State the blood parasite species.
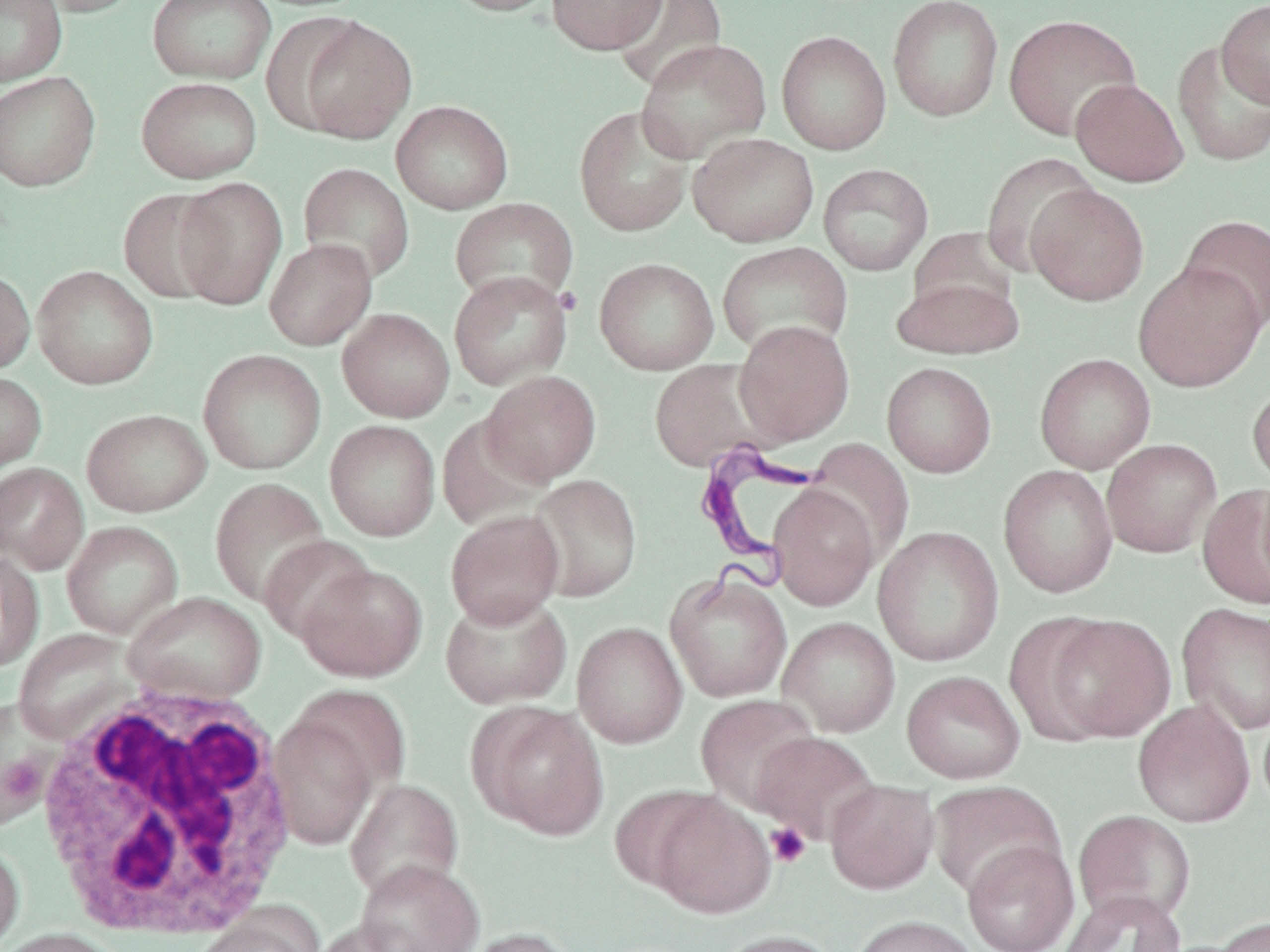

Trypanosoma brucei.

Summary:
  - Coordinate format: approximate bounding boxes as named x1/y1/x2/y2 corners in pixels
  - Trypanosoma brucei locations: (x1=687, y1=439, x2=826, y2=605)
  - Uninfected red blood cell locations: (x1=0, y1=0, x2=67, y2=86), (x1=32, y1=0, x2=144, y2=17), (x1=146, y1=0, x2=276, y2=84), (x1=442, y1=0, x2=562, y2=17), (x1=546, y1=0, x2=667, y2=54), (x1=610, y1=0, x2=728, y2=92), (x1=887, y1=0, x2=1004, y2=122), (x1=1216, y1=0, x2=1270, y2=108), (x1=1003, y1=14, x2=1141, y2=141), (x1=293, y1=15, x2=417, y2=143), (x1=776, y1=29, x2=891, y2=155), (x1=635, y1=38, x2=772, y2=163), (x1=1173, y1=41, x2=1270, y2=167), (x1=0, y1=71, x2=101, y2=191), (x1=136, y1=76, x2=262, y2=183), (x1=1070, y1=78, x2=1188, y2=186), (x1=391, y1=100, x2=513, y2=214), (x1=573, y1=105, x2=694, y2=237), (x1=687, y1=132, x2=819, y2=247), (x1=980, y1=153, x2=1100, y2=275), (x1=297, y1=163, x2=415, y2=284), (x1=817, y1=163, x2=934, y2=276), (x1=172, y1=176, x2=288, y2=310), (x1=1025, y1=184, x2=1149, y2=305), (x1=117, y1=187, x2=230, y2=303), (x1=449, y1=197, x2=579, y2=309), (x1=1179, y1=214, x2=1270, y2=332), (x1=907, y1=227, x2=1020, y2=323), (x1=264, y1=238, x2=377, y2=350), (x1=716, y1=241, x2=854, y2=358), (x1=594, y1=257, x2=719, y2=375), (x1=1133, y1=261, x2=1267, y2=392), (x1=32, y1=265, x2=158, y2=390), (x1=0, y1=268, x2=35, y2=375), (x1=448, y1=270, x2=573, y2=391), (x1=892, y1=273, x2=1024, y2=360), (x1=337, y1=308, x2=455, y2=422), (x1=734, y1=320, x2=855, y2=445), (x1=197, y1=348, x2=327, y2=475), (x1=1034, y1=353, x2=1155, y2=474), (x1=647, y1=357, x2=782, y2=472), (x1=881, y1=361, x2=997, y2=478), (x1=479, y1=370, x2=602, y2=485), (x1=0, y1=372, x2=47, y2=475), (x1=1248, y1=380, x2=1270, y2=491), (x1=81, y1=408, x2=212, y2=517), (x1=437, y1=413, x2=552, y2=528), (x1=325, y1=419, x2=440, y2=541), (x1=804, y1=438, x2=914, y2=564), (x1=1101, y1=439, x2=1221, y2=557), (x1=0, y1=462, x2=89, y2=574), (x1=998, y1=464, x2=1118, y2=597), (x1=526, y1=474, x2=643, y2=602), (x1=210, y1=478, x2=330, y2=606), (x1=1255, y1=478, x2=1270, y2=595), (x1=767, y1=484, x2=880, y2=610), (x1=1198, y1=486, x2=1270, y2=608), (x1=445, y1=509, x2=565, y2=627), (x1=61, y1=520, x2=183, y2=638), (x1=873, y1=526, x2=1004, y2=666), (x1=259, y1=534, x2=375, y2=645), (x1=0, y1=549, x2=44, y2=672), (x1=295, y1=562, x2=427, y2=681), (x1=664, y1=570, x2=793, y2=703), (x1=439, y1=591, x2=572, y2=710), (x1=122, y1=592, x2=267, y2=704), (x1=1177, y1=602, x2=1270, y2=735), (x1=1039, y1=613, x2=1176, y2=743), (x1=778, y1=616, x2=900, y2=737), (x1=572, y1=621, x2=687, y2=748), (x1=13, y1=629, x2=136, y2=743), (x1=901, y1=670, x2=1025, y2=784), (x1=289, y1=684, x2=413, y2=798), (x1=696, y1=694, x2=820, y2=812), (x1=0, y1=699, x2=61, y2=829), (x1=1132, y1=700, x2=1255, y2=827), (x1=470, y1=702, x2=608, y2=840), (x1=268, y1=712, x2=379, y2=851), (x1=750, y1=731, x2=880, y2=844), (x1=345, y1=778, x2=464, y2=901), (x1=825, y1=779, x2=939, y2=893), (x1=928, y1=781, x2=1065, y2=899), (x1=609, y1=785, x2=721, y2=894), (x1=648, y1=792, x2=775, y2=919), (x1=1073, y1=809, x2=1196, y2=926), (x1=0, y1=838, x2=24, y2=950), (x1=962, y1=840, x2=1079, y2=952), (x1=355, y1=860, x2=485, y2=952), (x1=1058, y1=890, x2=1185, y2=952), (x1=191, y1=908, x2=322, y2=952), (x1=849, y1=914, x2=981, y2=952), (x1=1212, y1=916, x2=1269, y2=952), (x1=310, y1=919, x2=424, y2=952), (x1=0, y1=927, x2=125, y2=952), (x1=458, y1=927, x2=582, y2=952), (x1=712, y1=929, x2=843, y2=952)
  - Platelet locations: (x1=765, y1=823, x2=811, y2=868)
  - White blood cell locations: (x1=32, y1=682, x2=304, y2=948)
  - Image size: 1270×952 pixels
  - Preparation: thin blood smear
  - Stain: May-Grünwald-Giemsa
  - Modality: optical microscopy
  - Magnification: 1000x
  - Field of view: one of a larger specimen